Identify the cell.
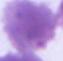

An erythrocyte.

{
  "modality": "micrograph",
  "magnification": "1000x"
}